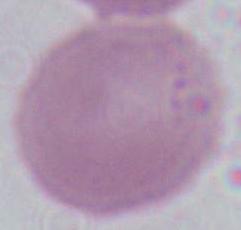

Summary:
  - Identification: red blood cell
  - Magnification: 1000x
  - Modality: micrograph